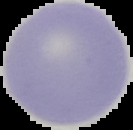
Segmented cell region on a black background. Malaria status: uninfected. Image is 133×130 pixels. From a thin blood smear.